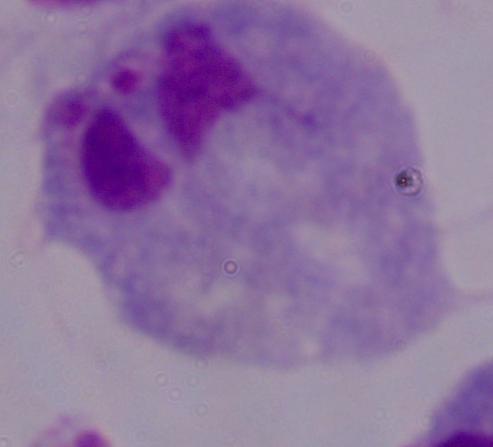
1000x magnification. A trichomonad is shown. Photomicrograph.